Classify this cell by malaria status.
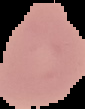
It is uninfected.

From a thin blood smear. Segmented cell region on a black background. Image is 85×109 pixels.